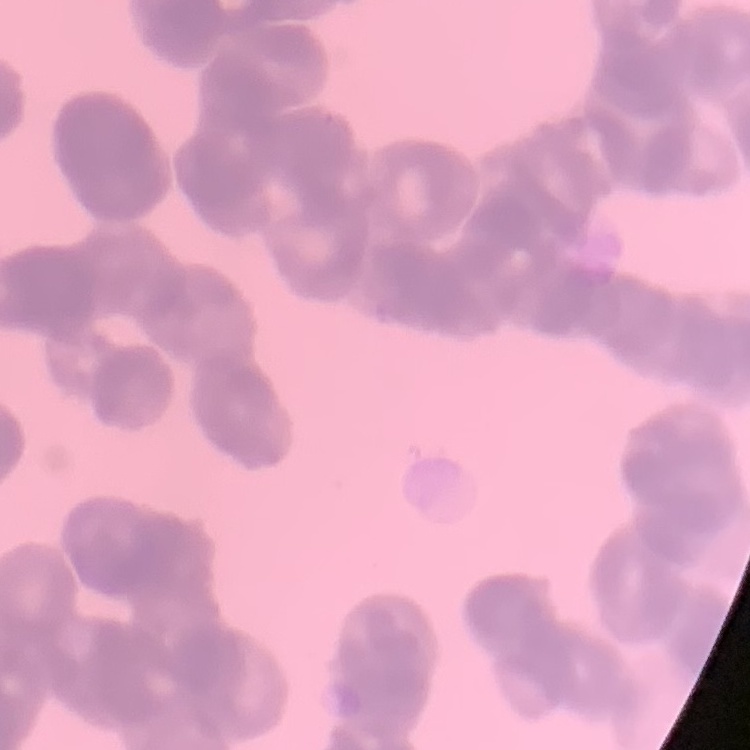

{
  "red_blood_cell_morphology": "rouleaux formation",
  "stain": "Field's or Giemsa",
  "preparation": "thin peripheral smear",
  "image_type": "one tile cut from a larger photomicrograph"
}